Name the blood parasite species.
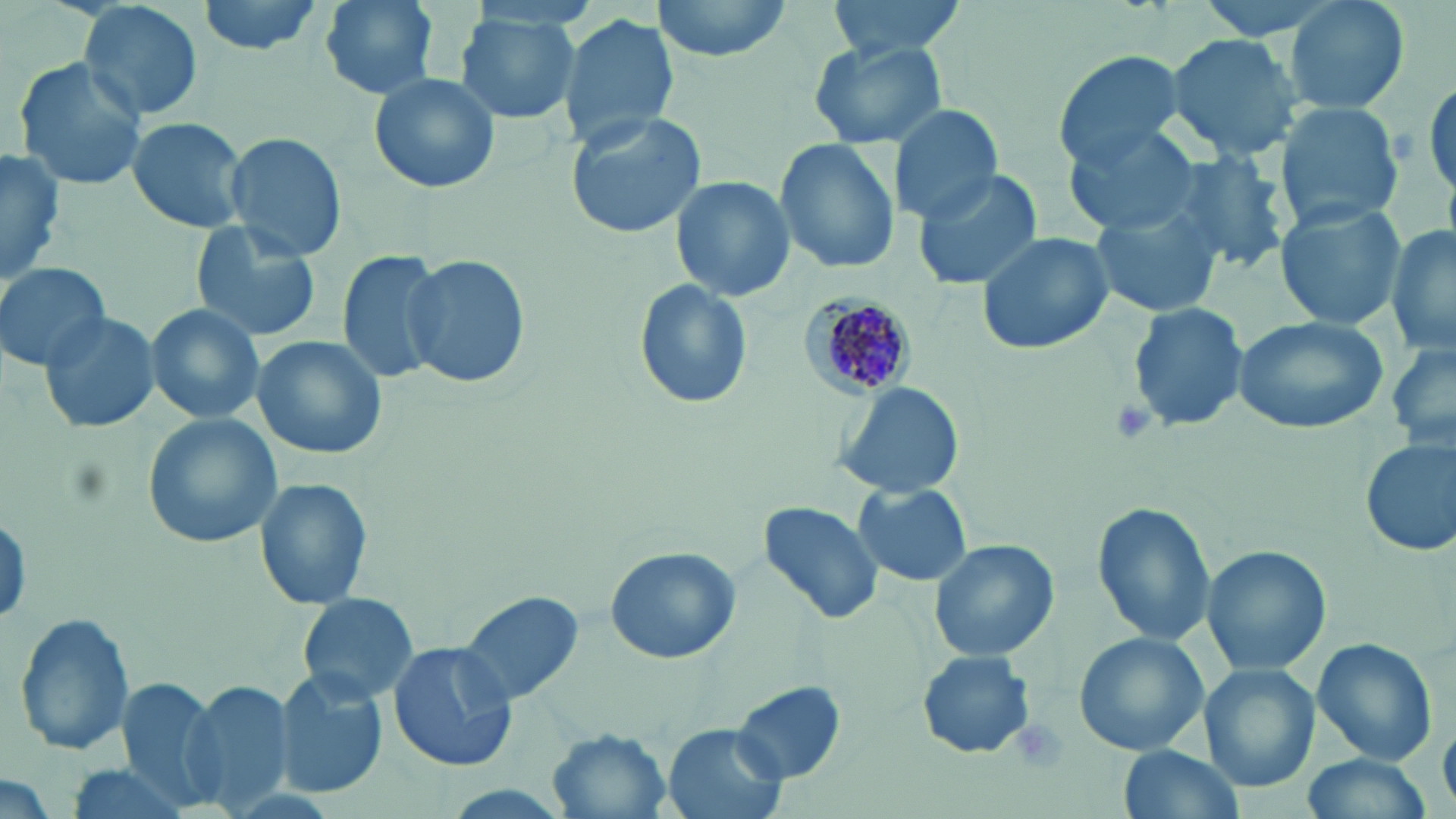

Plasmodium malariae.

Summary:
  - Coordinate format: approximate bounding boxes as named x1/y1/x2/y2 corners in pixels
  - Platelet locations: (x1=1107, y1=395, x2=1159, y2=445)
  - Plasmodium malariae-infected red blood cell locations: (x1=802, y1=292, x2=920, y2=399)
  - Uninfected red blood cell locations: (x1=78, y1=0, x2=205, y2=124), (x1=194, y1=0, x2=330, y2=56), (x1=314, y1=0, x2=444, y2=101), (x1=646, y1=0, x2=797, y2=63), (x1=824, y1=0, x2=968, y2=59), (x1=1282, y1=0, x2=1413, y2=117), (x1=453, y1=10, x2=585, y2=127), (x1=556, y1=12, x2=680, y2=151), (x1=1168, y1=32, x2=1305, y2=157), (x1=809, y1=39, x2=947, y2=148), (x1=1055, y1=52, x2=1187, y2=166), (x1=11, y1=56, x2=149, y2=191), (x1=368, y1=70, x2=500, y2=194), (x1=888, y1=102, x2=1006, y2=222), (x1=1273, y1=102, x2=1405, y2=231), (x1=567, y1=110, x2=707, y2=241), (x1=126, y1=115, x2=249, y2=234), (x1=1063, y1=122, x2=1204, y2=239), (x1=223, y1=131, x2=347, y2=260), (x1=774, y1=136, x2=900, y2=275), (x1=1166, y1=147, x2=1291, y2=274), (x1=1, y1=148, x2=64, y2=285), (x1=909, y1=168, x2=1048, y2=291), (x1=669, y1=174, x2=796, y2=304), (x1=1275, y1=200, x2=1407, y2=331), (x1=1091, y1=203, x2=1227, y2=317), (x1=189, y1=220, x2=323, y2=343), (x1=1387, y1=227, x2=1456, y2=357), (x1=975, y1=230, x2=1118, y2=356), (x1=334, y1=249, x2=445, y2=383), (x1=402, y1=254, x2=527, y2=390), (x1=0, y1=261, x2=112, y2=372), (x1=632, y1=279, x2=754, y2=409), (x1=145, y1=303, x2=267, y2=424), (x1=1129, y1=303, x2=1247, y2=432), (x1=39, y1=310, x2=160, y2=435), (x1=1235, y1=315, x2=1391, y2=434), (x1=251, y1=335, x2=385, y2=461), (x1=1387, y1=343, x2=1456, y2=453), (x1=833, y1=381, x2=964, y2=500), (x1=142, y1=412, x2=281, y2=548), (x1=1359, y1=435, x2=1455, y2=559), (x1=255, y1=476, x2=374, y2=611), (x1=853, y1=482, x2=972, y2=586), (x1=1092, y1=501, x2=1214, y2=649), (x1=757, y1=503, x2=885, y2=625), (x1=929, y1=540, x2=1058, y2=661), (x1=1202, y1=544, x2=1330, y2=676), (x1=605, y1=546, x2=742, y2=665), (x1=457, y1=590, x2=588, y2=710), (x1=296, y1=592, x2=419, y2=707), (x1=14, y1=609, x2=137, y2=760), (x1=1073, y1=632, x2=1210, y2=757), (x1=1313, y1=639, x2=1437, y2=765), (x1=387, y1=644, x2=519, y2=773), (x1=917, y1=651, x2=1034, y2=757), (x1=1201, y1=662, x2=1321, y2=792), (x1=275, y1=670, x2=389, y2=797), (x1=117, y1=679, x2=220, y2=798), (x1=183, y1=681, x2=292, y2=810), (x1=732, y1=682, x2=847, y2=783), (x1=662, y1=724, x2=788, y2=819), (x1=548, y1=730, x2=671, y2=817), (x1=1118, y1=743, x2=1242, y2=819), (x1=1298, y1=752, x2=1437, y2=817), (x1=55, y1=763, x2=201, y2=819), (x1=0, y1=772, x2=61, y2=819)
  - Stain: May-Grünwald-Giemsa
  - Preparation: thin blood film
  - Magnification: 1000x
  - Modality: light microscopy
  - Image size: 1456×819 pixels
  - Field of view: one of a larger specimen